Report the malaria status of this cell.
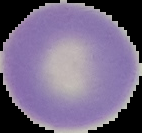

It is uninfected.

{
  "image_type": "segmented cell region on a black background",
  "image_size": "142×133 pixels",
  "preparation": "thin blood film"
}